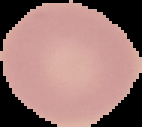
preparation = thin blood film
image size = 142×127 pixels
result = negative for Plasmodium parasites
image type = segmented cell region on a black background